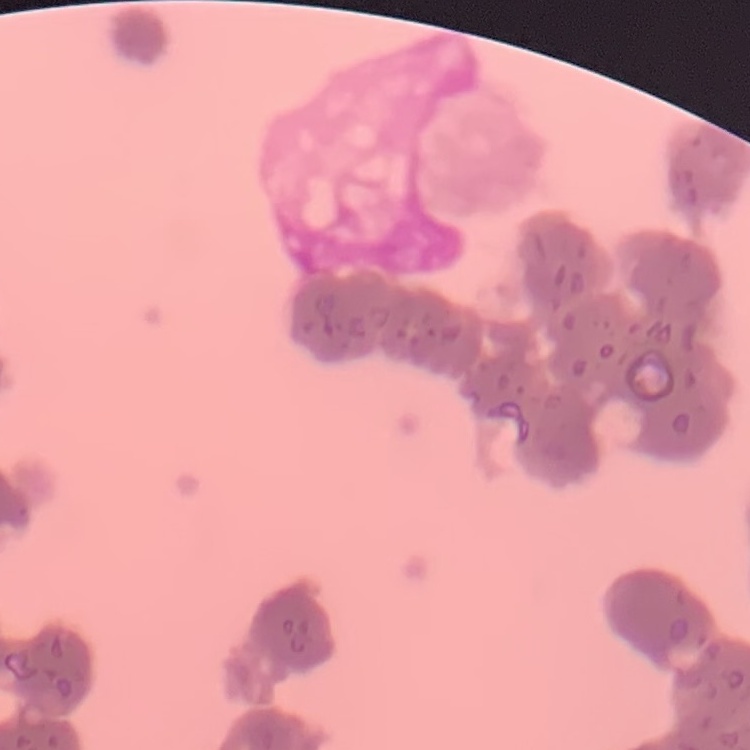

erythrocyte morphology = rouleaux formation
image type = one tile cut from a larger photomicrograph
preparation = thin peripheral smear
stain = Field's or Giemsa